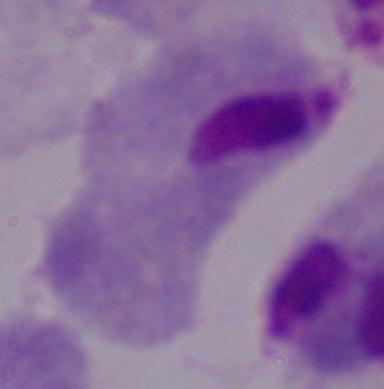
Summary:
  - Magnification: 1000x
  - Identification: trichomonad
  - Modality: photomicrograph